Outline each blood parasite and name the species.
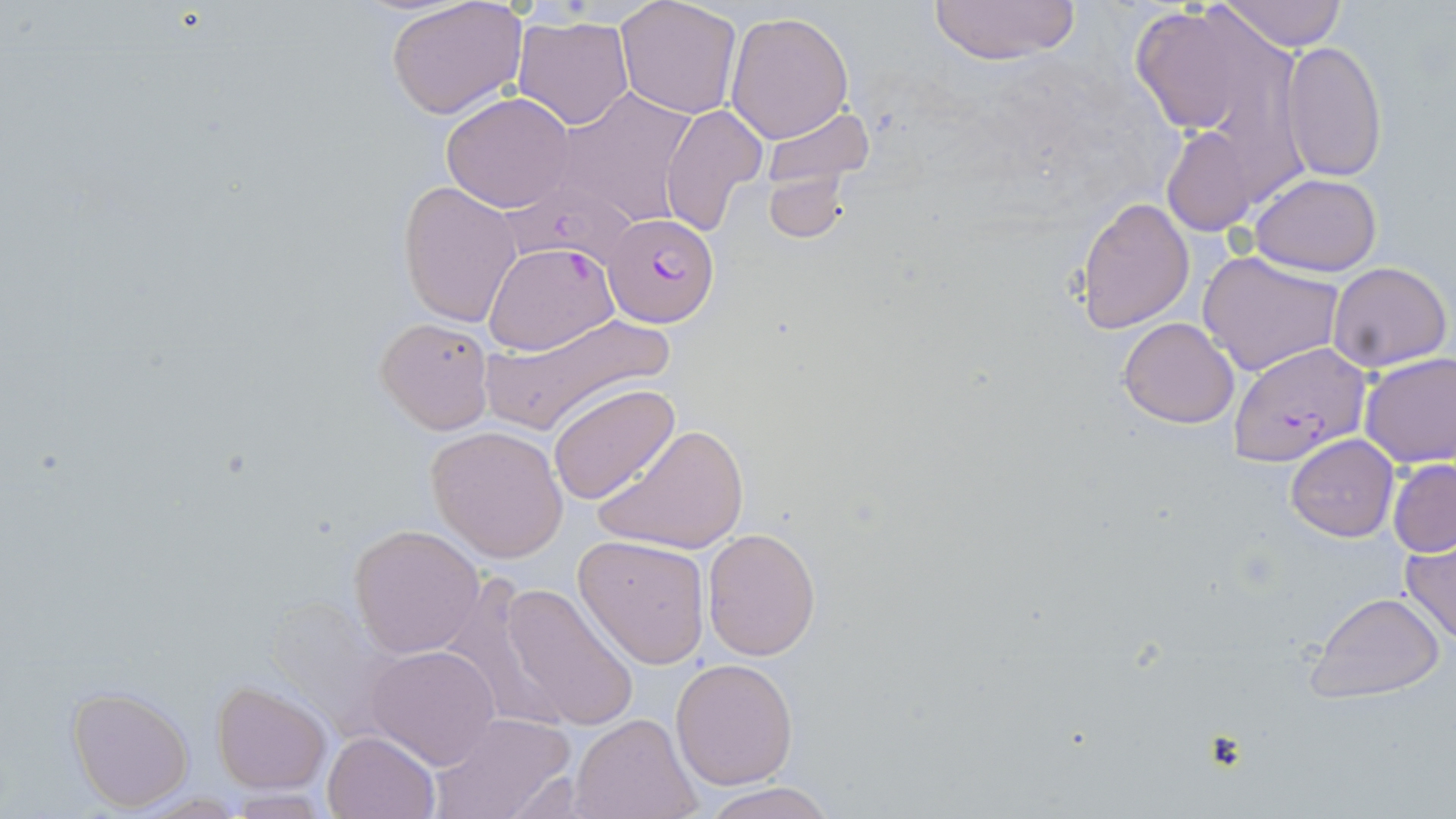

Approximate bounding boxes as (x1, y1, x2, y2) in pixels.
Plasmodium falciparum-infected red blood cells: (603, 213, 720, 329), (483, 241, 622, 353), (1229, 341, 1370, 466).
No Plasmodium ovale, Plasmodium malariae, Plasmodium vivax, Babesia divergens, or Trypanosoma brucei observed.

{
  "slide_level_diagnosis": "Plasmodium falciparum",
  "field_of_view": "one of a larger specimen",
  "modality": "light microscopy",
  "uninfected_red_blood_cell_locations": "approximate bounding boxes as (x1, y1, x2, y2) in pixels: (386, 0, 529, 120), (925, 0, 1081, 66), (1221, 0, 1347, 50), (614, 1, 743, 118), (1128, 2, 1286, 145), (724, 9, 855, 145), (513, 15, 635, 131), (1279, 39, 1388, 183), (552, 89, 702, 230), (441, 91, 575, 212), (659, 103, 768, 237), (756, 107, 876, 197), (1161, 125, 1259, 236), (763, 169, 854, 244), (1250, 172, 1384, 274), (399, 180, 524, 327), (1074, 196, 1195, 332), (1196, 248, 1345, 377), (1327, 260, 1452, 371), (482, 311, 668, 432), (374, 315, 495, 432), (1117, 317, 1240, 428), (1358, 351, 1456, 468), (548, 382, 679, 505), (592, 421, 750, 555), (426, 425, 568, 561), (1285, 433, 1398, 542), (1387, 457, 1456, 558), (350, 525, 484, 657), (703, 528, 820, 660), (574, 534, 712, 667), (1399, 540, 1456, 645), (498, 582, 639, 732), (1307, 591, 1446, 702), (365, 644, 502, 769), (669, 658, 797, 790), (212, 681, 331, 793), (67, 685, 196, 811), (428, 711, 575, 819), (570, 714, 698, 819), (323, 730, 438, 818), (697, 781, 843, 819)",
  "preparation": "thin blood smear",
  "magnification": "1000x",
  "stain": "May-Grünwald-Giemsa",
  "image_size": "1456×819 pixels"
}